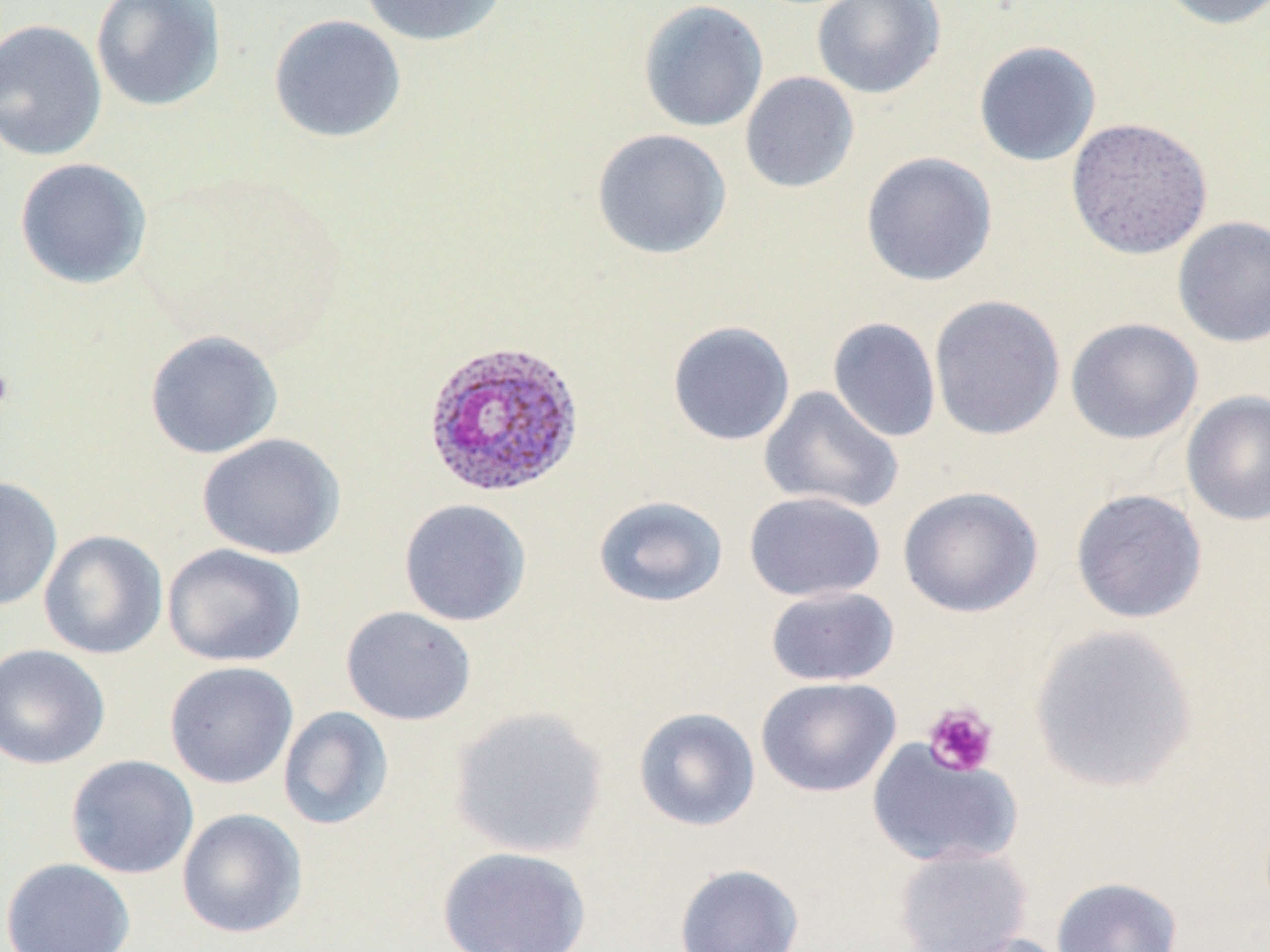
Summary:
  - Coordinate format: approximate bounding boxes as [x1, y1, x2, y2] in pixels
  - Uninfected red blood cell locations: [90, 0, 226, 112], [357, 0, 508, 46], [810, 0, 945, 99], [1152, 0, 1270, 31], [638, 1, 769, 132], [268, 14, 406, 144], [0, 19, 107, 162], [973, 40, 1102, 167], [739, 71, 860, 194], [1064, 117, 1213, 259], [591, 128, 732, 259], [860, 151, 998, 287], [14, 157, 152, 290], [1171, 215, 1270, 348], [928, 294, 1066, 441], [827, 316, 941, 443], [1065, 317, 1203, 445], [667, 320, 795, 446], [144, 329, 284, 459], [758, 386, 903, 514], [1180, 390, 1270, 526], [197, 432, 346, 560], [0, 475, 63, 612], [897, 485, 1044, 619], [1070, 488, 1208, 624], [743, 491, 887, 602], [593, 495, 729, 607], [398, 498, 532, 626], [38, 529, 168, 660], [162, 543, 306, 667], [764, 586, 899, 687], [340, 605, 477, 726], [1029, 624, 1199, 794], [0, 643, 111, 770], [164, 661, 299, 790], [756, 676, 902, 798], [277, 705, 393, 830], [448, 706, 609, 858], [633, 706, 761, 831], [867, 740, 1021, 870], [65, 754, 199, 879], [176, 808, 308, 939], [893, 845, 1032, 952], [436, 846, 592, 952], [1, 858, 136, 952], [674, 862, 805, 952], [1051, 876, 1183, 952], [934, 932, 1073, 952]
  - Plasmodium ovale-infected red blood cell locations: [421, 338, 585, 499]
  - Platelet locations: [0, 361, 16, 418], [921, 702, 999, 777]
  - Slide-level diagnosis: Plasmodium ovale
  - Stain: May-Grünwald-Giemsa
  - Modality: optical microscopy
  - Field of view: single
  - Magnification: 1000x
  - Preparation: thin blood film
  - Image size: 1270×952 pixels